Report the malaria status of this cell.
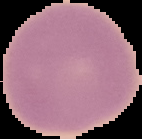

Uninfected.

Cell region segmented out of the field of view; the surrounding area is masked to black. Image is 142×139 pixels. From a thin blood smear.